Give the position of every Plasmodium parasite visible.
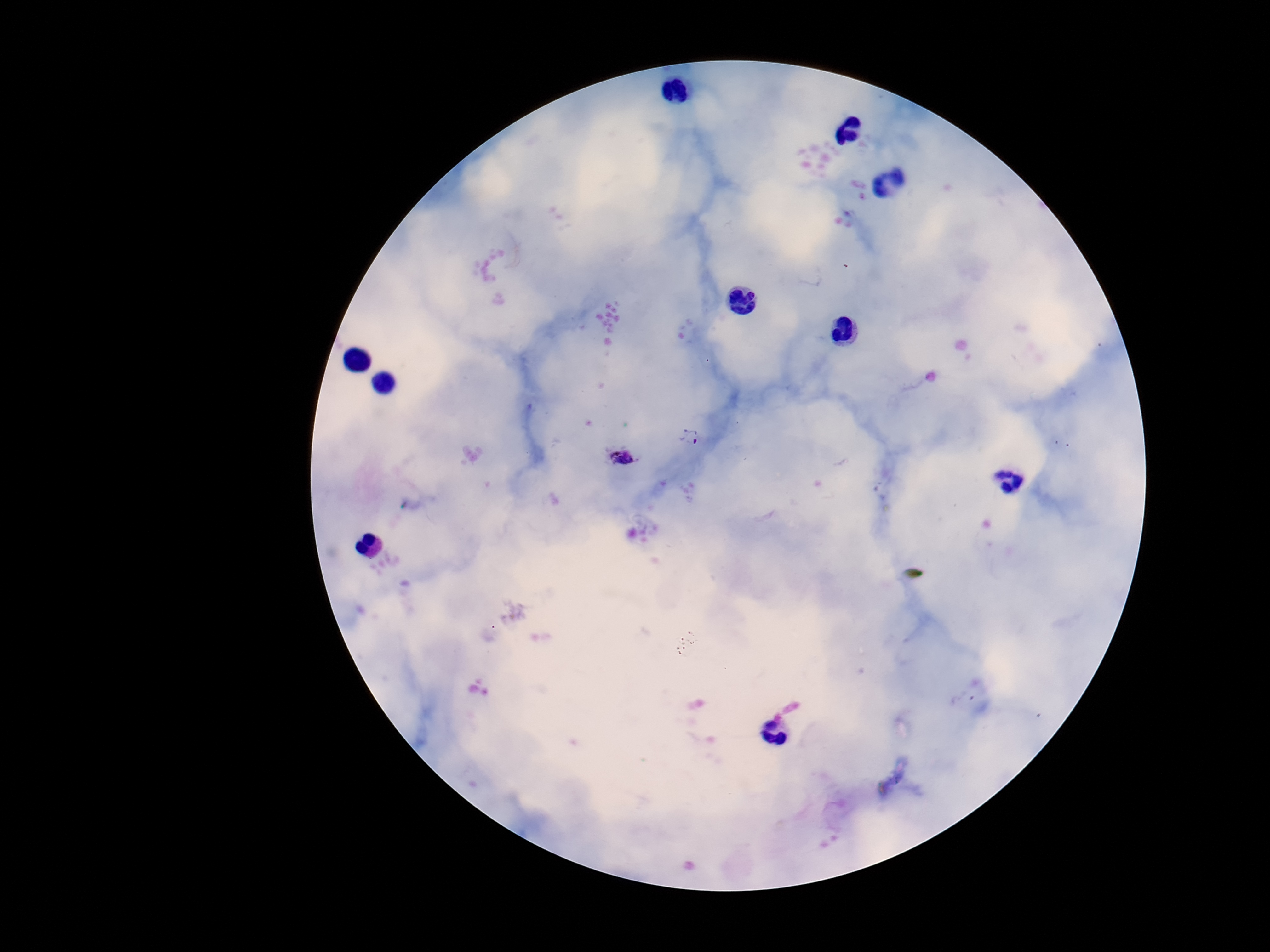
Approximate object centers, in pixels from the top-left corner.
Plasmodium parasites: (x=693, y=439), (x=621, y=456).

preparation = thick blood smear
patient malaria status = infected
magnification = 100x
field of view = one from this slide
image size = 1270×952 pixels
stain = Giemsa
capture = smartphone camera through the microscope eyepiece